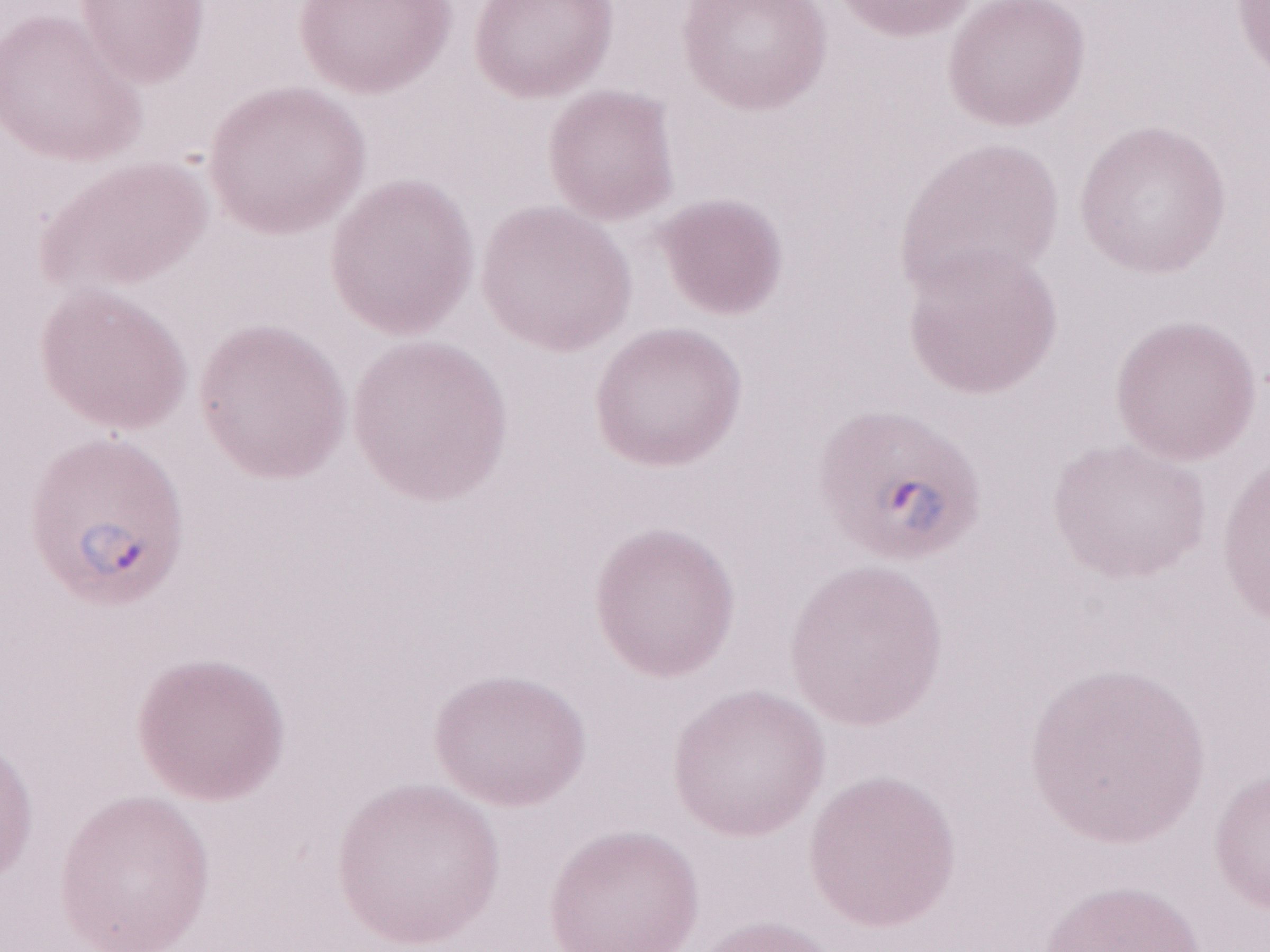
Image is 1270×952 pixels. Thin peripheral-blood smear. Patient-level malaria diagnosis: positive. May-Grünwald-Giemsa stain. Magnification: 1,000x. Olympus BX43 microscope, Olympus DP73 camera. One field of this slide.